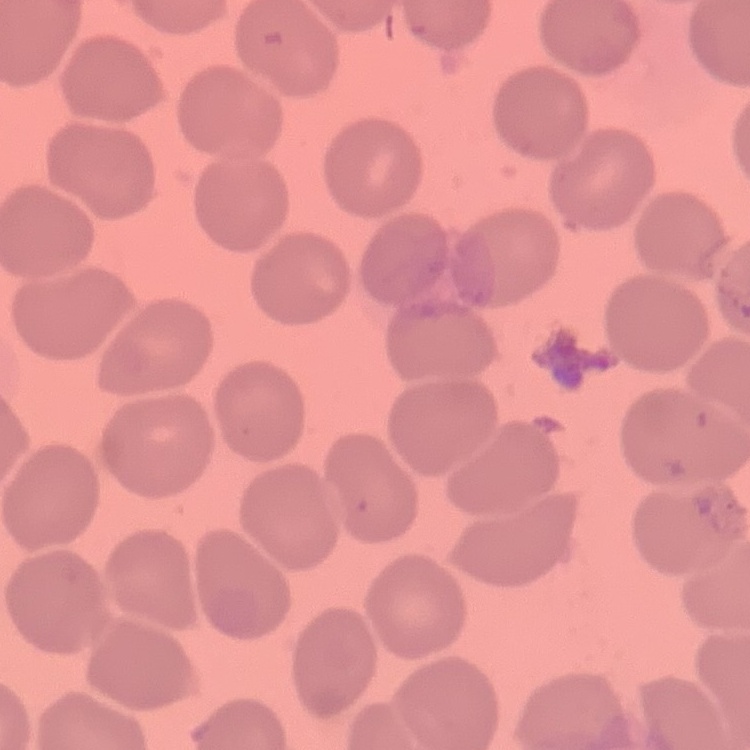

red blood cell morphology = no rouleaux formation
preparation = thin peripheral smear
stain = Field's or Giemsa
image type = one tile cut from a larger photomicrograph